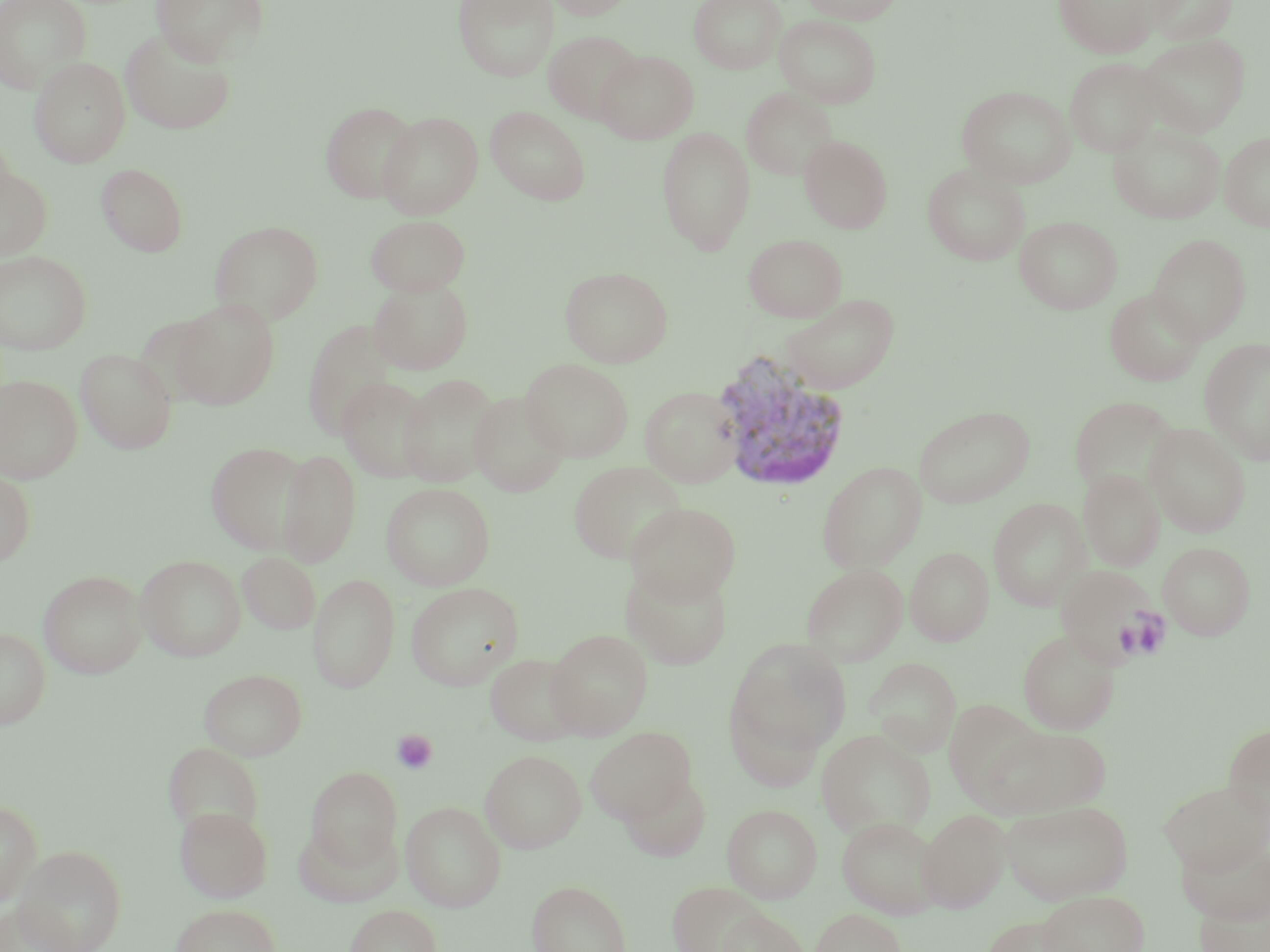
Approximate bounding boxes as (x1,y1)-(x2,y2) corner pairs in pixels. Uninfected red blood cell locations: (0,0)-(92,94), (150,0)-(270,66), (453,0)-(559,82), (546,0)-(636,20), (689,0)-(785,74), (799,0)-(905,24), (1055,0)-(1158,58), (1144,0)-(1236,45), (689,4)-(881,83), (775,14)-(882,107), (120,28)-(237,136), (544,29)-(644,124), (1136,33)-(1250,136), (595,50)-(698,143), (1064,57)-(1165,157), (30,58)-(131,167), (957,85)-(1076,188), (741,87)-(838,181), (321,102)-(418,203), (485,106)-(590,205), (378,111)-(483,219), (1110,122)-(1225,223), (657,127)-(755,254), (1219,132)-(1270,231), (799,135)-(892,233), (96,163)-(188,256), (922,163)-(1031,265), (0,164)-(53,260), (366,215)-(470,296), (1015,215)-(1122,314), (210,220)-(324,325), (743,233)-(847,322), (1147,233)-(1252,344), (0,250)-(92,354), (560,266)-(673,367), (369,279)-(473,375), (1105,288)-(1205,386), (781,292)-(900,395), (172,298)-(280,409), (302,319)-(400,441), (1200,337)-(1270,465), (75,348)-(178,454), (521,358)-(633,462), (397,373)-(501,486), (0,374)-(82,484), (338,376)-(436,482), (640,386)-(743,487), (468,391)-(570,497), (1070,396)-(1179,495), (913,405)-(1035,509), (1146,423)-(1251,537), (205,441)-(310,554), (278,449)-(361,567), (568,461)-(686,564), (817,461)-(926,572), (1078,469)-(1165,570), (0,471)-(36,567), (381,482)-(495,590), (989,498)-(1091,610), (625,502)-(740,604), (1158,542)-(1255,640), (905,546)-(993,646), (237,551)-(321,635), (136,554)-(246,661), (620,563)-(734,670), (801,563)-(908,666), (1055,564)-(1161,668), (39,569)-(147,678), (308,573)-(400,693), (405,582)-(523,690), (0,627)-(51,729), (546,629)-(653,738), (1018,630)-(1120,734), (727,638)-(852,760), (485,653)-(585,746), (865,657)-(961,756), (200,668)-(306,760), (725,693)-(827,791), (942,698)-(1048,809), (986,724)-(1111,818), (1223,724)-(1270,824), (586,727)-(695,823), (817,730)-(935,840), (164,741)-(263,835), (480,749)-(586,852), (306,766)-(402,869), (618,771)-(712,862), (1159,779)-(1270,875), (0,798)-(42,908), (401,800)-(506,912), (1001,800)-(1132,904), (722,803)-(822,903), (174,805)-(273,903), (917,809)-(1011,913), (836,816)-(942,918), (295,819)-(401,909), (14,844)-(127,952), (527,880)-(631,952), (667,880)-(769,952), (1037,890)-(1149,952), (1194,890)-(1270,952), (0,901)-(79,952), (169,903)-(281,952), (344,904)-(442,952), (714,908)-(810,952), (810,908)-(906,952), (978,914)-(1082,952). Plasmodium vivax-infected red blood cell locations: (711,353)-(853,493). Platelet locations: (1124,609)-(1172,660), (391,729)-(438,775). Slide-level diagnosis: Plasmodium vivax. Single field of view. May-Grünwald-Giemsa-stained preparation. Thin blood smear. 1000x magnification. Light microscopy. Image is 1270×952 pixels.